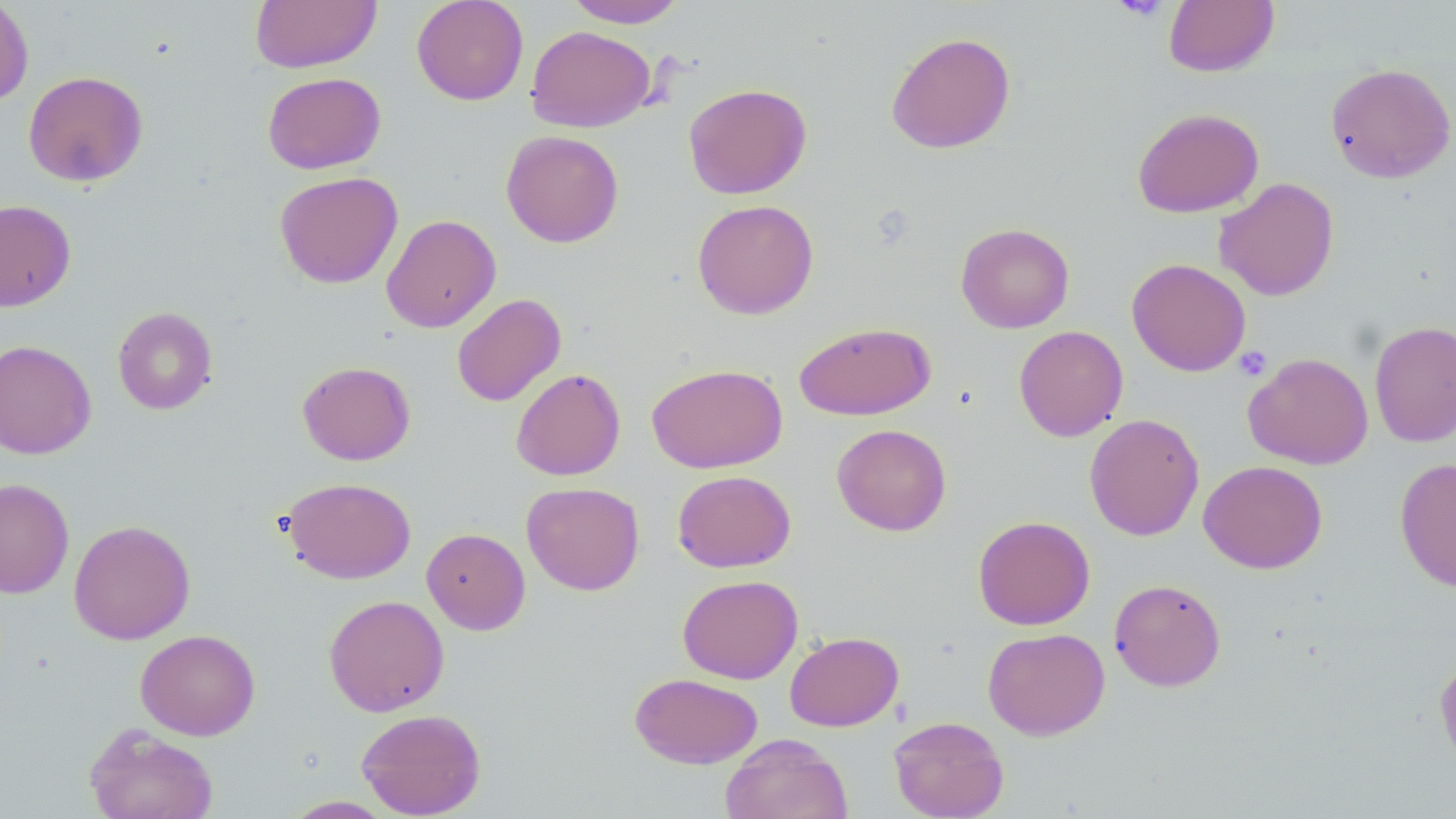
{
  "slide_level_diagnosis": "negative for blood parasites",
  "uninfected_red_blood_cell_locations": "approximate bounding boxes as [x1, y1, x2, y2] in pixels: [0, 0, 34, 107], [250, 0, 381, 73], [411, 0, 528, 105], [564, 0, 687, 28], [1163, 0, 1279, 77], [526, 25, 655, 132], [885, 31, 1016, 154], [1325, 62, 1456, 184], [23, 70, 148, 187], [262, 71, 386, 174], [683, 83, 811, 199], [1132, 107, 1264, 218], [501, 130, 623, 247], [274, 171, 403, 289], [1214, 177, 1339, 301], [692, 199, 819, 319], [0, 200, 76, 311], [381, 214, 501, 332], [955, 222, 1075, 333], [1126, 258, 1251, 377], [451, 293, 566, 407], [112, 306, 218, 415], [1369, 320, 1456, 448], [793, 321, 936, 420], [1013, 325, 1128, 441], [0, 339, 97, 459], [1244, 352, 1374, 470], [297, 360, 416, 465], [646, 363, 788, 473], [511, 368, 626, 481], [1084, 413, 1204, 541], [831, 423, 952, 536], [1395, 457, 1456, 592], [1198, 460, 1327, 573], [672, 470, 796, 573], [281, 477, 416, 584], [0, 478, 74, 598], [522, 481, 644, 596], [973, 515, 1095, 630], [69, 519, 195, 644], [421, 527, 531, 635], [677, 574, 803, 684], [1109, 578, 1226, 691], [324, 594, 449, 716], [982, 627, 1110, 739], [135, 629, 260, 741], [784, 631, 904, 732], [1434, 653, 1456, 773], [629, 672, 762, 769], [356, 708, 486, 818], [889, 715, 1009, 819], [84, 723, 218, 819], [719, 733, 852, 819], [282, 796, 395, 818]",
  "field_of_view": "one of a larger specimen",
  "image_size": "1456×819 pixels",
  "magnification": "1000x",
  "platelet_locations": "approximate bounding boxes as [x1, y1, x2, y2] in pixels: [1111, 0, 1172, 20], [1233, 346, 1272, 381]",
  "stain": "May-Grünwald-Giemsa",
  "modality": "optical microscopy",
  "preparation": "thin blood film"
}